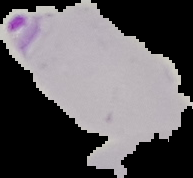

image type = cell region segmented out of the field of view; surrounding area masked to black
malaria status = parasitized
preparation = thin blood smear
image size = 193×178 pixels